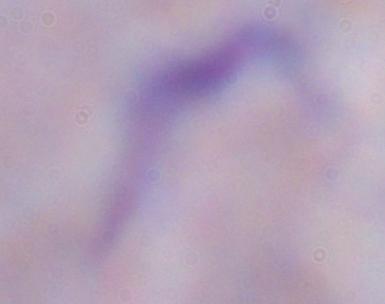
{
  "identification": "trypanosome",
  "magnification": "1000x",
  "modality": "photomicrograph"
}